Name the parasite shown.
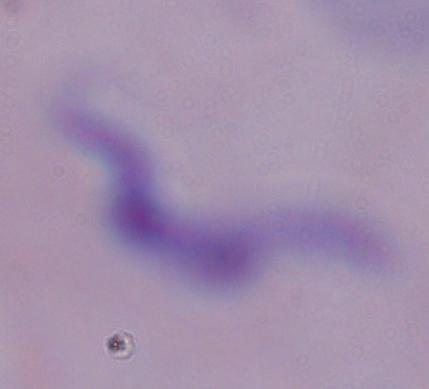
A trypanosome.

modality = micrograph
magnification = 1000x